State the blood parasite species.
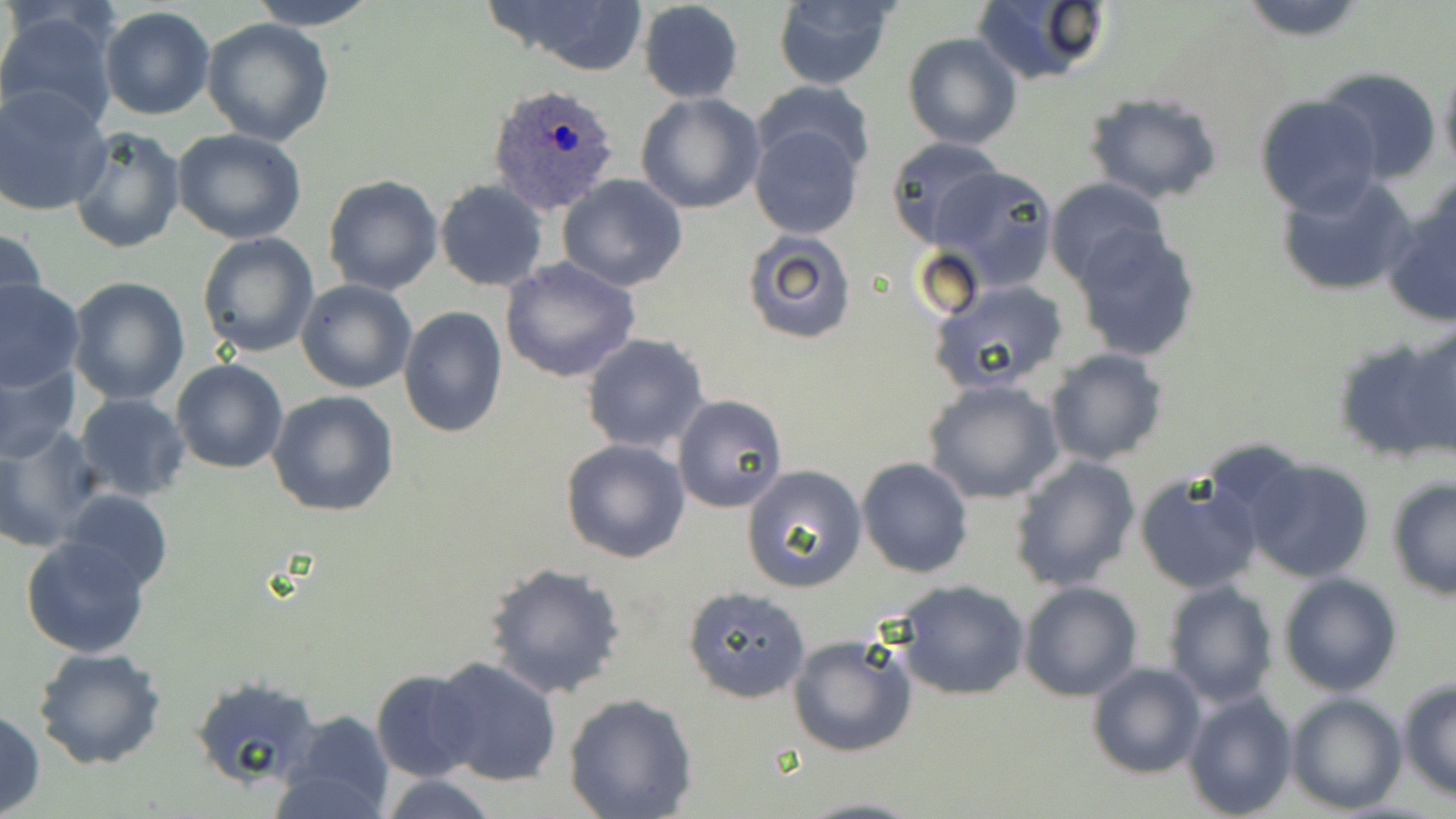

Plasmodium ovale.

Summary:
  - Coordinate format: approximate bounding boxes as (x1,y1)-(x2,y2) corner pairs in pixels
  - Plasmodium ovale-infected red blood cell locations: (489,83)-(622,214)
  - Uninfected red blood cell locations: (244,0)-(382,30), (481,0)-(651,76), (768,0)-(902,89), (971,0)-(1112,87), (1235,0)-(1372,40), (637,2)-(745,104), (99,7)-(215,121), (0,8)-(121,133), (201,18)-(334,146), (902,32)-(1023,149), (1437,55)-(1456,184), (1318,67)-(1441,187), (752,80)-(876,176), (1,86)-(112,217), (1082,91)-(1224,205), (635,92)-(766,214), (1255,94)-(1384,217), (749,122)-(863,239), (68,127)-(185,254), (173,128)-(307,244), (884,138)-(1006,250), (931,164)-(1058,291), (1274,173)-(1418,298), (322,174)-(445,294), (558,175)-(690,292), (1045,176)-(1169,286), (434,181)-(549,291), (1385,184)-(1455,327), (1070,224)-(1204,360), (2,225)-(46,331), (740,229)-(858,346), (196,231)-(321,358), (499,257)-(640,384), (68,276)-(190,404), (0,278)-(84,391), (297,279)-(417,395), (929,279)-(1071,396), (398,307)-(508,437), (1342,323)-(1456,466), (581,335)-(710,455), (1043,348)-(1168,466), (0,357)-(81,461), (171,358)-(288,474), (922,379)-(1065,504), (268,391)-(401,516), (73,393)-(191,501), (675,395)-(787,513), (0,427)-(101,553), (560,438)-(690,565), (1010,455)-(1141,591), (857,457)-(974,578), (1244,457)-(1375,582), (741,464)-(869,594), (1134,472)-(1263,596), (1387,478)-(1455,600), (63,489)-(173,593), (20,535)-(151,659), (483,562)-(628,701), (1278,572)-(1402,696), (896,579)-(1030,700), (1018,580)-(1141,701), (1161,580)-(1280,707), (682,586)-(811,703), (787,633)-(916,758), (32,646)-(168,770), (429,656)-(561,787), (1087,663)-(1206,779), (371,668)-(485,781), (190,676)-(321,790), (1397,680)-(1456,800), (1181,689)-(1299,818), (1284,691)-(1407,814), (564,693)-(698,818), (0,707)-(43,815), (275,709)-(396,819), (375,775)-(499,818), (793,796)-(927,819)
  - Magnification: 1000x
  - Stain: May-Grünwald-Giemsa
  - Image size: 1456×819 pixels
  - Modality: optical microscopy
  - Field of view: single
  - Preparation: thin blood smear